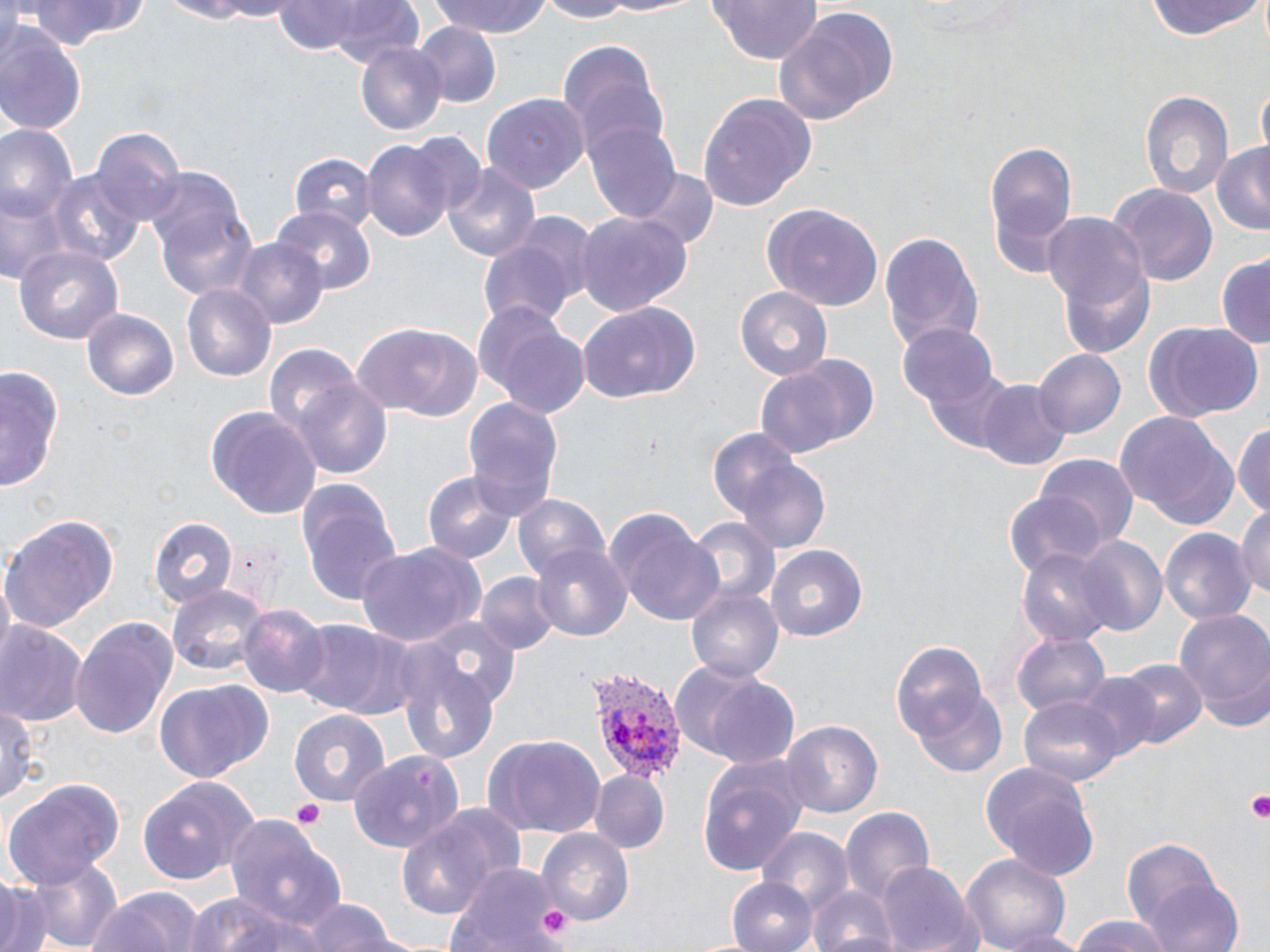

Approximate bounding boxes as named x1/y1/x2/y2 corners in pixels. Platelet locations: (x1=1243, y1=790, x2=1270, y2=824), (x1=292, y1=798, x2=327, y2=830), (x1=537, y1=904, x2=576, y2=945). Plasmodium vivax-infected red blood cell locations: (x1=590, y1=669, x2=685, y2=783). Uninfected red blood cell locations: (x1=21, y1=0, x2=147, y2=48), (x1=149, y1=0, x2=276, y2=23), (x1=428, y1=0, x2=554, y2=39), (x1=534, y1=0, x2=636, y2=23), (x1=600, y1=0, x2=710, y2=18), (x1=705, y1=0, x2=824, y2=66), (x1=270, y1=1, x2=424, y2=65), (x1=1144, y1=1, x2=1263, y2=41), (x1=774, y1=8, x2=898, y2=126), (x1=0, y1=23, x2=87, y2=132), (x1=415, y1=24, x2=500, y2=105), (x1=557, y1=40, x2=669, y2=155), (x1=356, y1=42, x2=447, y2=137), (x1=1256, y1=83, x2=1270, y2=158), (x1=1140, y1=90, x2=1231, y2=198), (x1=697, y1=92, x2=813, y2=210), (x1=480, y1=93, x2=586, y2=191), (x1=582, y1=117, x2=683, y2=222), (x1=0, y1=126, x2=78, y2=221), (x1=91, y1=128, x2=183, y2=229), (x1=981, y1=134, x2=1080, y2=282), (x1=364, y1=137, x2=455, y2=243), (x1=1211, y1=144, x2=1270, y2=234), (x1=290, y1=152, x2=375, y2=230), (x1=443, y1=165, x2=544, y2=262), (x1=145, y1=166, x2=256, y2=299), (x1=46, y1=169, x2=143, y2=270), (x1=633, y1=169, x2=717, y2=254), (x1=1112, y1=185, x2=1218, y2=288), (x1=2, y1=187, x2=68, y2=284), (x1=763, y1=203, x2=885, y2=310), (x1=272, y1=205, x2=377, y2=292), (x1=572, y1=208, x2=691, y2=315), (x1=1043, y1=213, x2=1145, y2=310), (x1=879, y1=231, x2=983, y2=356), (x1=476, y1=233, x2=585, y2=332), (x1=230, y1=238, x2=325, y2=328), (x1=15, y1=244, x2=124, y2=346), (x1=1214, y1=255, x2=1270, y2=350), (x1=1058, y1=262, x2=1158, y2=359), (x1=182, y1=281, x2=276, y2=380), (x1=735, y1=286, x2=834, y2=383), (x1=578, y1=299, x2=703, y2=405), (x1=80, y1=306, x2=180, y2=401), (x1=474, y1=307, x2=591, y2=418), (x1=1143, y1=322, x2=1263, y2=422), (x1=352, y1=324, x2=484, y2=421), (x1=898, y1=325, x2=1001, y2=417), (x1=264, y1=346, x2=362, y2=438), (x1=1034, y1=348, x2=1126, y2=439), (x1=752, y1=353, x2=879, y2=457), (x1=1, y1=365, x2=63, y2=496), (x1=294, y1=380, x2=393, y2=478), (x1=978, y1=380, x2=1071, y2=472), (x1=462, y1=396, x2=564, y2=519), (x1=205, y1=406, x2=323, y2=520), (x1=1115, y1=412, x2=1241, y2=530), (x1=1234, y1=421, x2=1270, y2=522), (x1=733, y1=454, x2=835, y2=558), (x1=1036, y1=455, x2=1139, y2=551), (x1=423, y1=470, x2=518, y2=567), (x1=293, y1=474, x2=402, y2=609), (x1=1003, y1=491, x2=1107, y2=580), (x1=514, y1=494, x2=610, y2=584), (x1=606, y1=506, x2=723, y2=624), (x1=1234, y1=508, x2=1270, y2=605), (x1=1, y1=517, x2=118, y2=636), (x1=149, y1=517, x2=236, y2=611), (x1=689, y1=518, x2=778, y2=610), (x1=1162, y1=527, x2=1254, y2=628), (x1=1072, y1=536, x2=1166, y2=635), (x1=354, y1=541, x2=485, y2=649), (x1=530, y1=542, x2=634, y2=642), (x1=766, y1=543, x2=870, y2=643), (x1=1017, y1=547, x2=1116, y2=650), (x1=475, y1=572, x2=560, y2=657), (x1=167, y1=582, x2=270, y2=678), (x1=685, y1=583, x2=783, y2=682), (x1=236, y1=604, x2=328, y2=697), (x1=1173, y1=610, x2=1270, y2=729), (x1=70, y1=615, x2=179, y2=739), (x1=419, y1=616, x2=521, y2=710), (x1=288, y1=620, x2=422, y2=722), (x1=0, y1=623, x2=86, y2=731), (x1=1014, y1=633, x2=1110, y2=721), (x1=892, y1=642, x2=992, y2=748), (x1=395, y1=649, x2=502, y2=765), (x1=1119, y1=660, x2=1204, y2=747), (x1=676, y1=661, x2=803, y2=767), (x1=1073, y1=673, x2=1163, y2=762), (x1=153, y1=679, x2=273, y2=784), (x1=911, y1=687, x2=1010, y2=778), (x1=0, y1=696, x2=38, y2=809), (x1=1020, y1=696, x2=1121, y2=787), (x1=289, y1=709, x2=393, y2=806), (x1=781, y1=718, x2=884, y2=822), (x1=481, y1=733, x2=606, y2=839), (x1=350, y1=750, x2=466, y2=854), (x1=697, y1=753, x2=810, y2=878), (x1=979, y1=761, x2=1102, y2=878), (x1=590, y1=771, x2=668, y2=854), (x1=139, y1=774, x2=261, y2=887), (x1=3, y1=778, x2=124, y2=888), (x1=838, y1=803, x2=936, y2=907), (x1=225, y1=809, x2=347, y2=939), (x1=393, y1=810, x2=511, y2=922), (x1=757, y1=829, x2=853, y2=915), (x1=539, y1=830, x2=636, y2=926), (x1=1121, y1=837, x2=1234, y2=946), (x1=22, y1=852, x2=124, y2=952), (x1=958, y1=852, x2=1072, y2=952), (x1=879, y1=861, x2=980, y2=951), (x1=446, y1=862, x2=566, y2=950), (x1=1144, y1=876, x2=1247, y2=952), (x1=729, y1=878, x2=812, y2=951), (x1=0, y1=882, x2=47, y2=952), (x1=809, y1=885, x2=897, y2=952), (x1=88, y1=886, x2=208, y2=952), (x1=181, y1=892, x2=318, y2=952), (x1=304, y1=898, x2=399, y2=951), (x1=1065, y1=915, x2=1178, y2=952), (x1=996, y1=927, x2=1088, y2=952). Slide-level diagnosis: Plasmodium vivax. One field of a larger specimen. Thin blood film. Optical microscopy. 1000x magnification. Image is 1270×952 pixels. May-Grünwald-Giemsa stain.